Assess the morphology of the red blood cells.
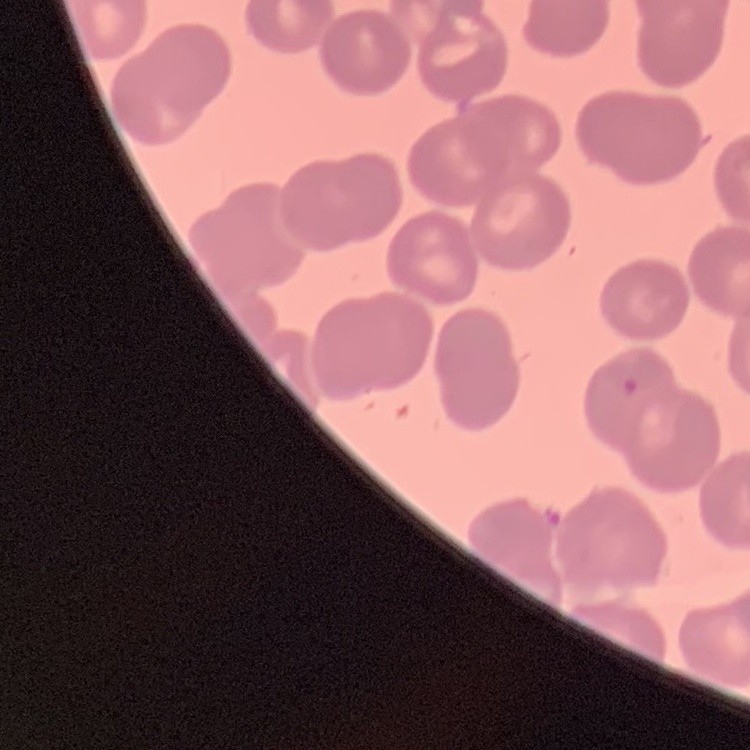

They show no rouleaux formation.

One tile cut from a larger photomicrograph. Thin blood smear. Stained with either Field's or Giemsa.